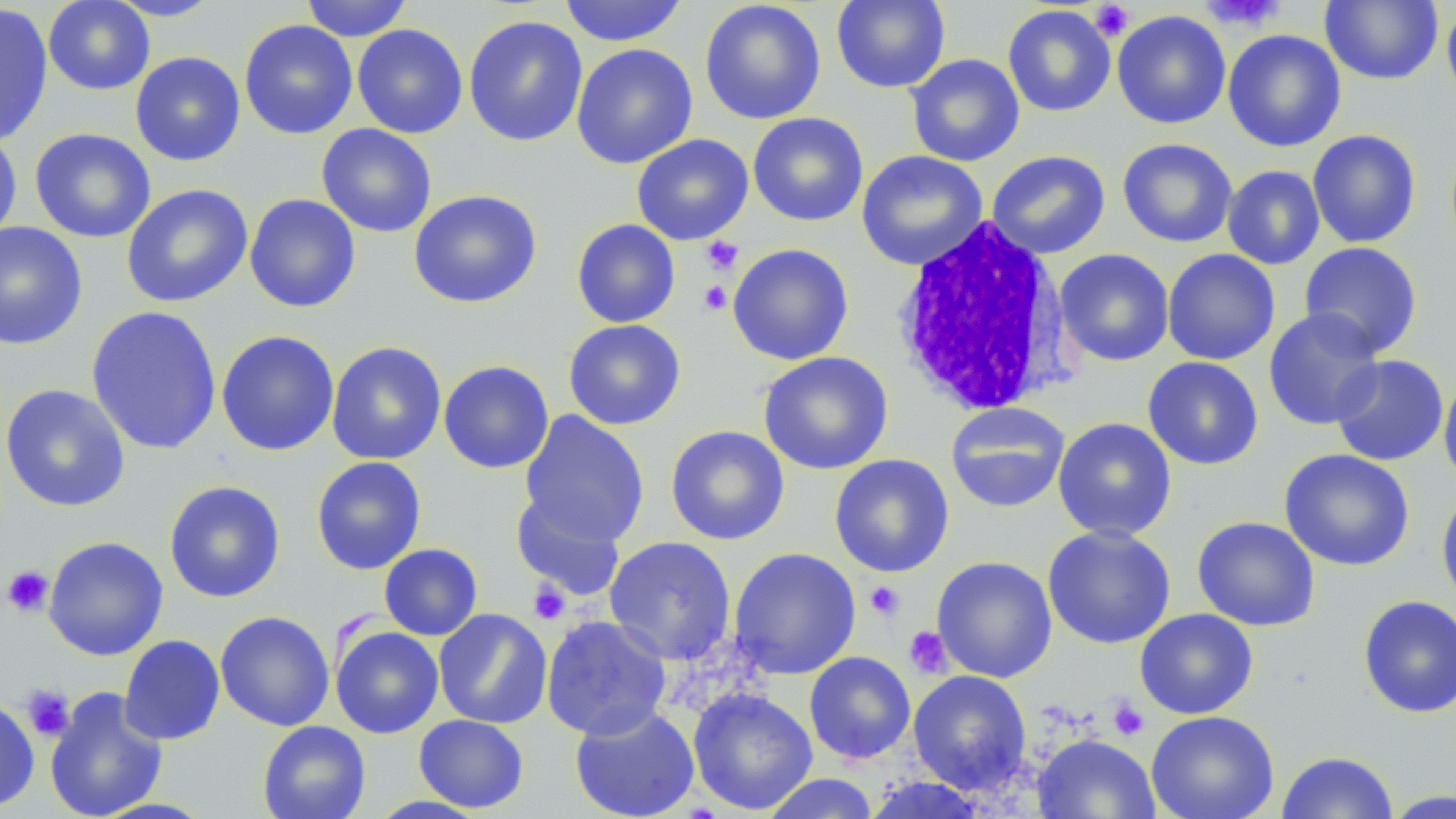

slide-level diagnosis = negative for blood parasites
platelet locations = approximate bounding boxes as named x1/y1/x2/y2 corners in pixels: (x1=1200, y1=0, x2=1286, y2=30), (x1=1090, y1=2, x2=1135, y2=41), (x1=701, y1=236, x2=743, y2=275), (x1=699, y1=281, x2=731, y2=314), (x1=2, y1=565, x2=54, y2=618), (x1=528, y1=580, x2=571, y2=624), (x1=864, y1=581, x2=905, y2=621), (x1=904, y1=626, x2=952, y2=679), (x1=20, y1=684, x2=73, y2=742), (x1=1106, y1=697, x2=1149, y2=742)
white blood cell locations = approximate bounding boxes as named x1/y1/x2/y2 corners in pixels: (x1=891, y1=215, x2=1074, y2=418)
magnification = 1000x
field of view = single
image size = 1456×819 pixels
uninfected red blood cell locations = approximate bounding boxes as named x1/y1/x2/y2 corners in pixels: (x1=43, y1=0, x2=154, y2=95), (x1=105, y1=0, x2=224, y2=21), (x1=300, y1=0, x2=412, y2=41), (x1=558, y1=0, x2=688, y2=47), (x1=700, y1=0, x2=826, y2=124), (x1=831, y1=0, x2=950, y2=93), (x1=1320, y1=0, x2=1443, y2=86), (x1=0, y1=4, x2=53, y2=147), (x1=1442, y1=4, x2=1456, y2=110), (x1=1003, y1=5, x2=1116, y2=117), (x1=1112, y1=10, x2=1231, y2=130), (x1=463, y1=15, x2=588, y2=147), (x1=239, y1=19, x2=358, y2=140), (x1=352, y1=24, x2=468, y2=139), (x1=1222, y1=30, x2=1347, y2=152), (x1=572, y1=43, x2=698, y2=169), (x1=130, y1=51, x2=245, y2=166), (x1=906, y1=54, x2=1025, y2=167), (x1=748, y1=112, x2=868, y2=227), (x1=316, y1=123, x2=437, y2=238), (x1=30, y1=128, x2=156, y2=243), (x1=1307, y1=129, x2=1421, y2=248), (x1=0, y1=130, x2=22, y2=245), (x1=632, y1=134, x2=754, y2=245), (x1=1117, y1=138, x2=1238, y2=248), (x1=856, y1=150, x2=988, y2=271), (x1=987, y1=150, x2=1111, y2=259), (x1=1222, y1=165, x2=1325, y2=270), (x1=121, y1=184, x2=253, y2=308), (x1=408, y1=189, x2=542, y2=308), (x1=245, y1=193, x2=360, y2=313), (x1=571, y1=219, x2=680, y2=328), (x1=0, y1=221, x2=87, y2=350), (x1=1299, y1=241, x2=1423, y2=359), (x1=727, y1=243, x2=854, y2=365), (x1=1162, y1=248, x2=1280, y2=366), (x1=1054, y1=249, x2=1174, y2=367), (x1=86, y1=305, x2=222, y2=455), (x1=1264, y1=307, x2=1385, y2=430), (x1=563, y1=319, x2=686, y2=430), (x1=216, y1=330, x2=339, y2=456), (x1=326, y1=341, x2=447, y2=464), (x1=758, y1=351, x2=893, y2=475), (x1=1328, y1=354, x2=1450, y2=467), (x1=1142, y1=356, x2=1264, y2=470), (x1=438, y1=359, x2=554, y2=474), (x1=1438, y1=373, x2=1456, y2=490), (x1=1, y1=384, x2=130, y2=512), (x1=945, y1=402, x2=1070, y2=513), (x1=519, y1=410, x2=650, y2=547), (x1=1052, y1=417, x2=1177, y2=541), (x1=666, y1=425, x2=789, y2=545), (x1=1278, y1=449, x2=1416, y2=571), (x1=829, y1=454, x2=955, y2=578), (x1=311, y1=456, x2=426, y2=575), (x1=164, y1=480, x2=286, y2=603), (x1=1436, y1=489, x2=1456, y2=610), (x1=510, y1=491, x2=626, y2=600), (x1=1192, y1=516, x2=1321, y2=631), (x1=1042, y1=525, x2=1176, y2=650), (x1=43, y1=536, x2=168, y2=660), (x1=604, y1=536, x2=737, y2=664), (x1=379, y1=543, x2=482, y2=641), (x1=729, y1=547, x2=861, y2=679), (x1=932, y1=556, x2=1058, y2=682), (x1=1358, y1=595, x2=1456, y2=719), (x1=434, y1=608, x2=553, y2=728), (x1=1135, y1=609, x2=1259, y2=719), (x1=215, y1=611, x2=335, y2=731), (x1=540, y1=615, x2=672, y2=740), (x1=330, y1=625, x2=444, y2=738), (x1=119, y1=634, x2=225, y2=745), (x1=804, y1=651, x2=916, y2=764), (x1=908, y1=670, x2=1032, y2=794), (x1=44, y1=687, x2=168, y2=819), (x1=688, y1=687, x2=818, y2=815), (x1=0, y1=696, x2=39, y2=812), (x1=570, y1=704, x2=700, y2=819), (x1=1146, y1=710, x2=1279, y2=819), (x1=414, y1=713, x2=529, y2=813), (x1=257, y1=721, x2=371, y2=819), (x1=1032, y1=733, x2=1161, y2=819), (x1=1276, y1=751, x2=1398, y2=818), (x1=760, y1=773, x2=881, y2=819), (x1=862, y1=775, x2=992, y2=818), (x1=1381, y1=789, x2=1456, y2=818)
preparation = thin blood film
modality = light microscopy
stain = May-Grünwald-Giemsa